Classify this cell by malaria status.
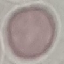
It is uninfected.

Summary:
  - Capture: smartphone camera at the microscope eyepiece
  - Stain: Giemsa
  - Preparation: thin smear
  - Image type: cell patch, automatically extracted from a larger field of view and resized to 64 × 64 pixels